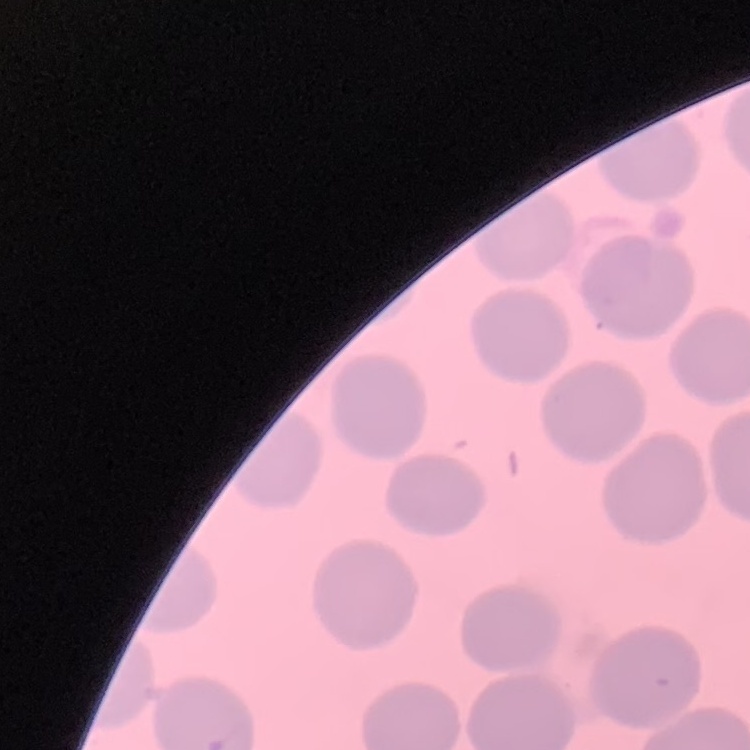

erythrocyte morphology = no rouleaux formation
preparation = thin blood smear
image type = square crop of a larger photomicrograph
stain = Field's or Giemsa